State which cell type is depicted.
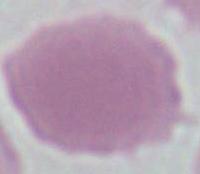

An erythrocyte.

Summary:
  - Modality: photomicrograph
  - Magnification: 1000x